Locate every Plasmodium parasite.
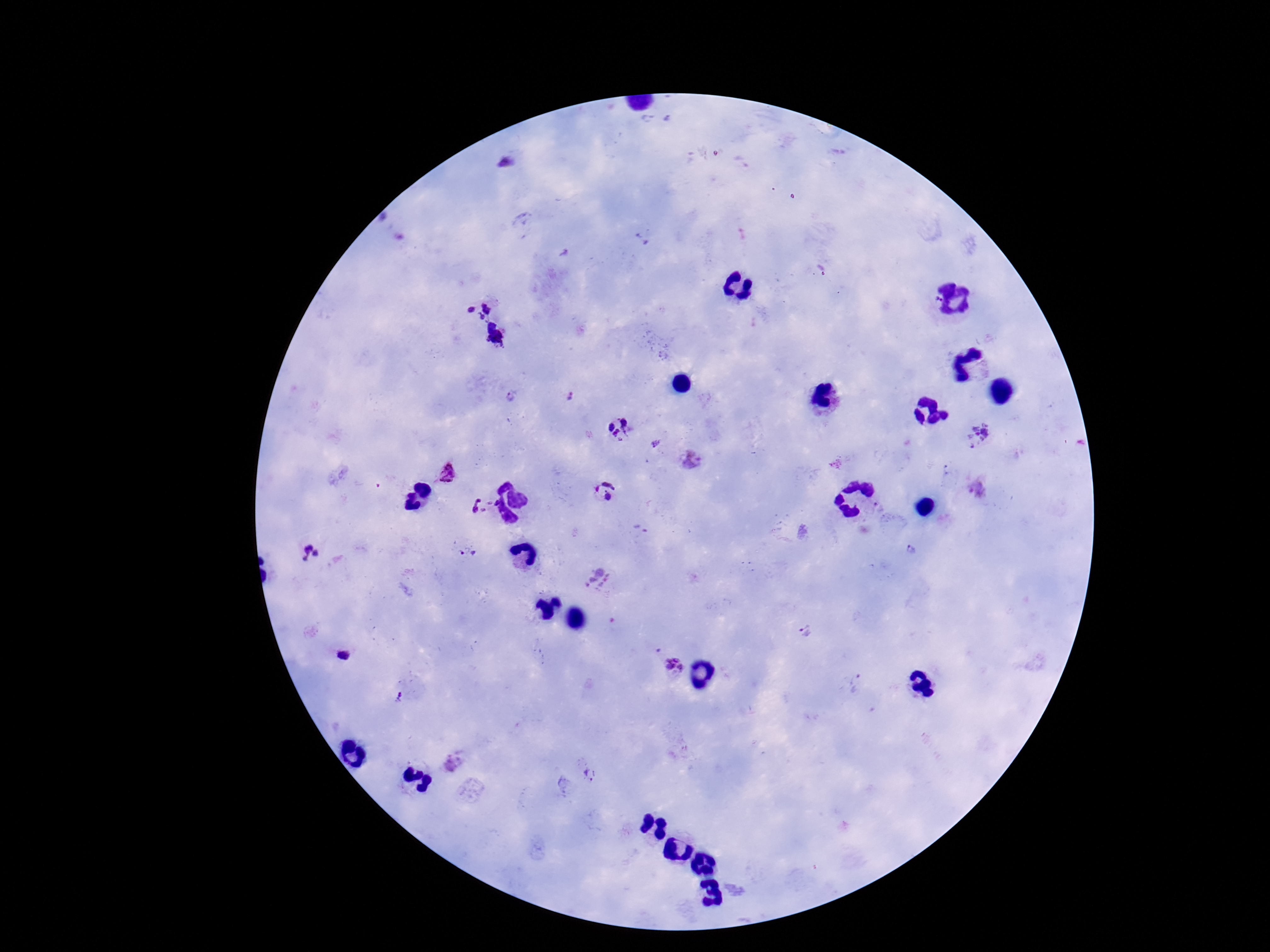

Approximate centers as (x, y) in pixels.
Plasmodium parasites: (505, 160), (641, 240), (481, 305), (497, 334), (567, 396), (510, 398), (618, 429), (978, 434), (656, 444), (691, 461), (448, 473), (978, 490), (604, 491), (476, 506), (910, 546), (467, 553), (310, 555), (597, 578), (805, 632), (342, 656), (672, 666), (855, 684), (400, 696), (453, 763), (588, 775).

preparation = thick blood smear
field of view = single
image size = 1270×952 pixels
magnification = 100x
patient malaria status = infected
capture = smartphone camera through the microscope eyepiece
stain = Giemsa